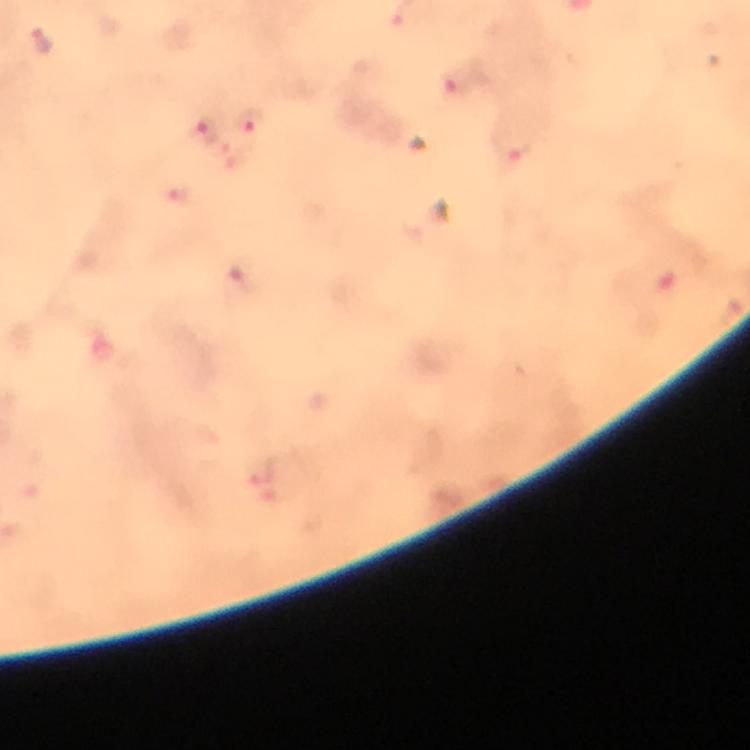

Approximate centers as (x, y) in pixels. Plasmodium parasite locations: (42, 42), (455, 79), (249, 122), (207, 132), (513, 147). At 100x magnification. Cropped region of a single field of view. Image is 750×750 pixels. Immersion oil applied. Thick blood smear. Photographed with a smartphone mounted on the microscope. From a diagnostic examination for malaria. Giemsa-stained preparation.